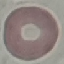

Malaria status: uninfected. Giemsa-stained preparation. Thin smear of blood. Photographed with a smartphone camera at the microscope eyepiece. Cell patch, automatically extracted from a larger field of view and resized to 64 × 64 pixels.